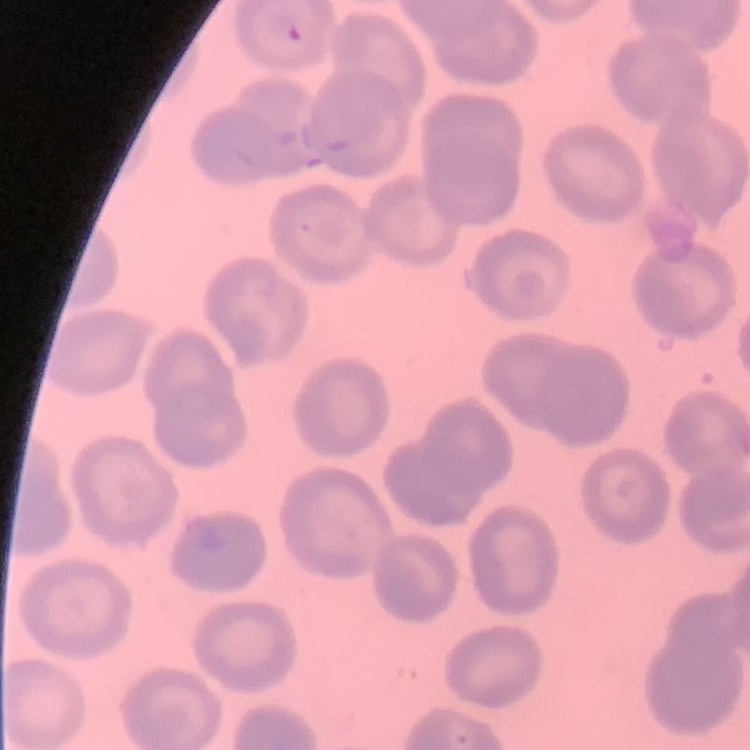

The erythrocytes show no rouleaux formation. Stained with either Field's or Giemsa. Square crop of a larger photomicrograph. Thin blood smear.